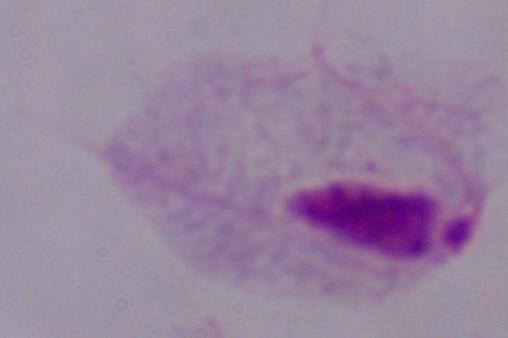

Summary:
  - Magnification: 1000x
  - Modality: micrograph
  - Identification: trichomonad